Identify the cell.
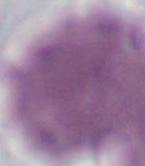

An erythrocyte.

Micrograph. Captured at 1000x magnification.